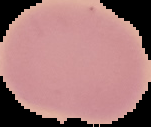
From a thin blood smear. The area outside the segmented cell region is set to black. Result: negative for Plasmodium parasites. Image is 151×127 pixels.